Give the extent of all uninfected red blood cells.
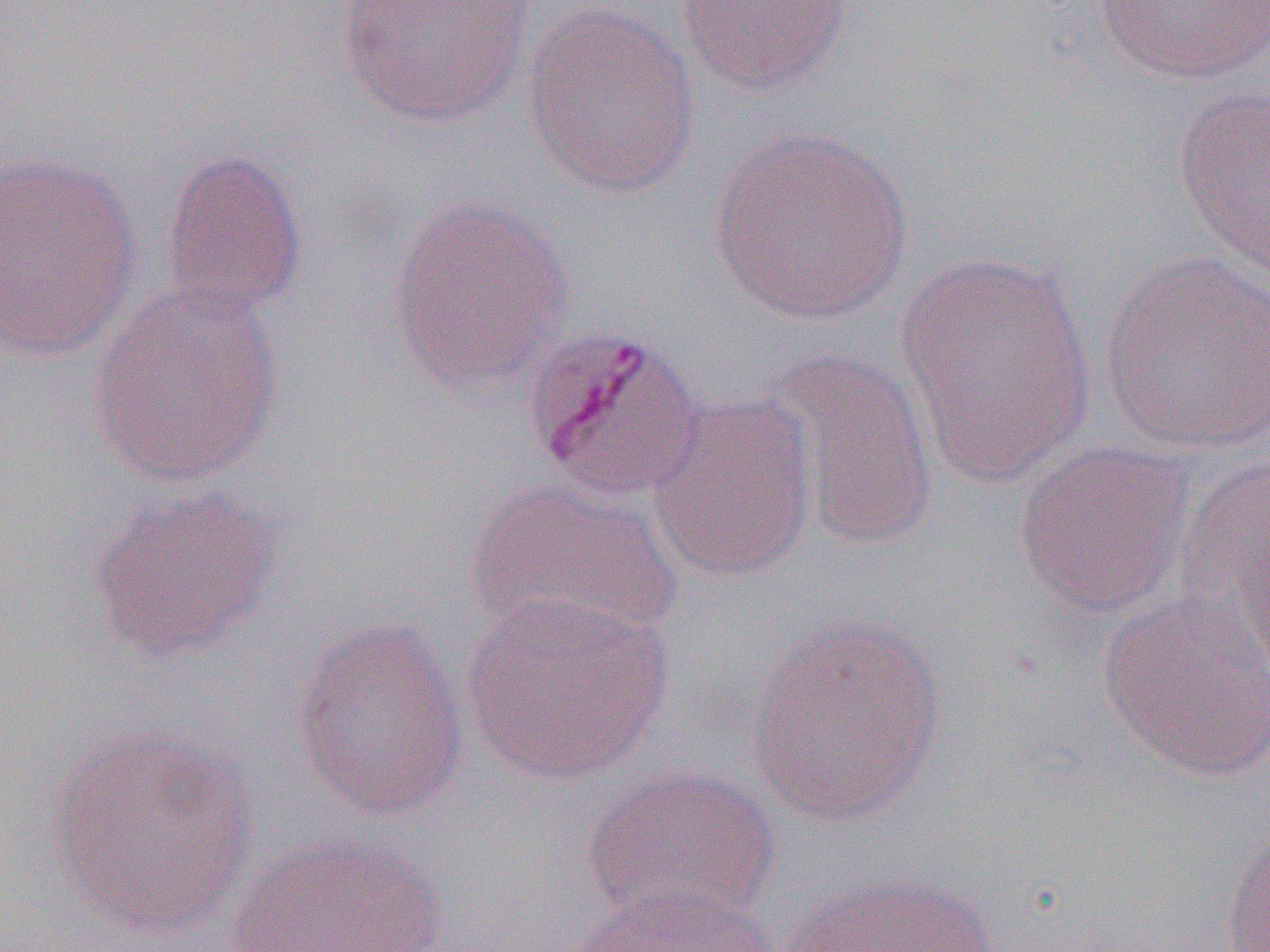
Approximate bounding boxes as (x1, y1, x2, y2) in pixels.
Uninfected red blood cells: (677, 0, 851, 96), (1093, 0, 1270, 86), (335, 1, 537, 127), (522, 3, 702, 199), (1172, 83, 1270, 277), (706, 127, 916, 325), (157, 145, 307, 321), (0, 153, 142, 365), (385, 193, 577, 397), (894, 249, 1097, 487), (1097, 251, 1270, 456), (87, 282, 284, 490), (523, 327, 705, 503), (761, 346, 941, 557), (646, 393, 818, 585), (1014, 439, 1197, 618), (1174, 452, 1270, 660), (462, 478, 680, 652), (86, 486, 281, 664), (1097, 587, 1270, 782), (459, 592, 673, 785), (744, 612, 952, 822), (290, 619, 469, 823), (43, 725, 258, 940), (582, 765, 780, 928), (1219, 826, 1270, 951), (223, 831, 450, 951), (774, 873, 999, 952), (561, 884, 780, 952).

Slide-level diagnosis: Plasmodium malariae. Image is 1270×952 pixels. 1000x magnification. Single field of view. Optical microscopy. Thin blood smear.